Report the malaria status of this cell.
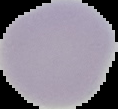
Uninfected.

{
  "preparation": "thin blood film",
  "image_size": "118×109 pixels",
  "image_type": "cell region segmented out of the field of view; surrounding area masked to black"
}